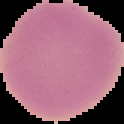
{
  "preparation": "thin blood smear",
  "image_type": "segmented cell region with the area outside set to black",
  "image_size": "124×124 pixels",
  "result": "no malaria parasites seen"
}